Locate every cell, classifying each as a parasitized red blood cell, an uninfected red blood cell, or a white blood cell.
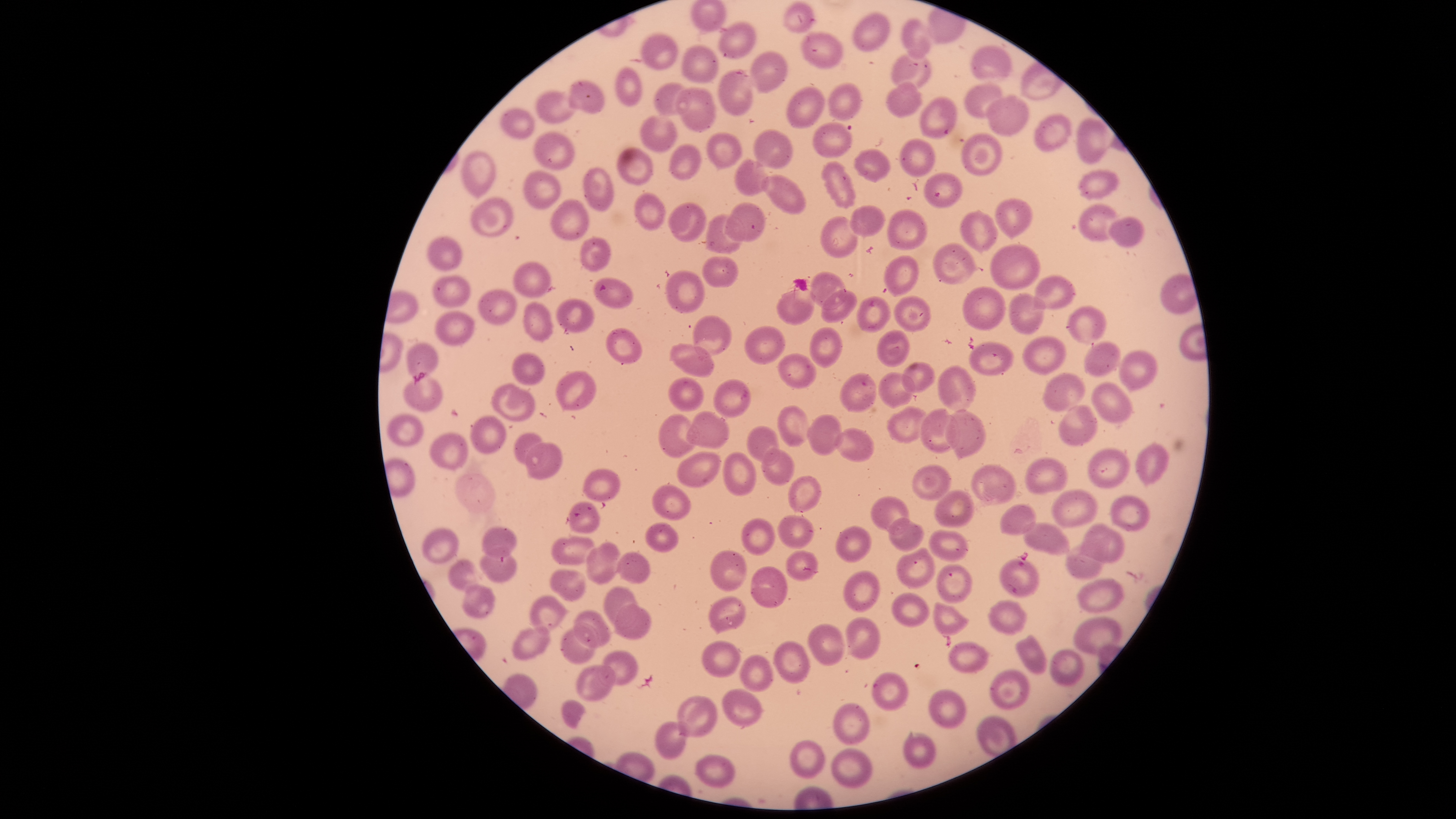
Approximate bounding boxes, in pixels from the top-left corner.
Parasitized red blood cells: (left=1000, top=557, right=1038, bottom=597).
Uninfected red blood cells: (left=690, top=0, right=727, bottom=32), (left=781, top=1, right=816, bottom=35), (left=852, top=13, right=891, bottom=53), (left=901, top=18, right=931, bottom=61), (left=718, top=22, right=757, bottom=59), (left=639, top=31, right=678, bottom=71), (left=800, top=31, right=844, bottom=69), (left=681, top=45, right=718, bottom=83), (left=971, top=45, right=1013, bottom=81), (left=750, top=51, right=787, bottom=93), (left=891, top=53, right=930, bottom=90), (left=615, top=68, right=643, bottom=106), (left=718, top=69, right=754, bottom=117), (left=567, top=80, right=606, bottom=114), (left=886, top=81, right=923, bottom=118), (left=653, top=82, right=693, bottom=117), (left=827, top=82, right=861, bottom=121), (left=962, top=84, right=1002, bottom=118), (left=786, top=86, right=825, bottom=130), (left=674, top=88, right=716, bottom=132), (left=536, top=90, right=577, bottom=124), (left=984, top=94, right=1029, bottom=136), (left=920, top=96, right=959, bottom=139), (left=499, top=108, right=536, bottom=140), (left=1034, top=113, right=1072, bottom=153), (left=639, top=114, right=678, bottom=153), (left=1076, top=118, right=1107, bottom=165), (left=813, top=122, right=852, bottom=158), (left=752, top=128, right=793, bottom=169), (left=534, top=131, right=575, bottom=170), (left=706, top=132, right=742, bottom=172), (left=961, top=133, right=1002, bottom=177), (left=899, top=139, right=935, bottom=178), (left=669, top=143, right=701, bottom=181), (left=617, top=147, right=653, bottom=186), (left=853, top=148, right=891, bottom=183), (left=461, top=150, right=498, bottom=199), (left=735, top=159, right=770, bottom=197), (left=820, top=160, right=856, bottom=210), (left=583, top=167, right=614, bottom=212), (left=1077, top=169, right=1119, bottom=200), (left=523, top=170, right=561, bottom=210), (left=923, top=171, right=964, bottom=209), (left=760, top=174, right=805, bottom=214), (left=633, top=192, right=667, bottom=231), (left=470, top=197, right=514, bottom=237), (left=995, top=198, right=1033, bottom=239), (left=551, top=199, right=590, bottom=241), (left=668, top=202, right=707, bottom=242), (left=724, top=202, right=766, bottom=242), (left=1079, top=204, right=1121, bottom=241), (left=850, top=205, right=885, bottom=240), (left=888, top=208, right=927, bottom=251), (left=960, top=209, right=999, bottom=256), (left=705, top=214, right=745, bottom=254), (left=821, top=216, right=858, bottom=258), (left=1108, top=217, right=1145, bottom=247), (left=426, top=234, right=461, bottom=271), (left=580, top=239, right=612, bottom=271), (left=931, top=243, right=979, bottom=285), (left=990, top=244, right=1040, bottom=290), (left=883, top=255, right=919, bottom=297), (left=701, top=256, right=739, bottom=288), (left=513, top=262, right=553, bottom=298), (left=664, top=269, right=705, bottom=314), (left=809, top=271, right=847, bottom=309), (left=432, top=275, right=471, bottom=307), (left=1033, top=275, right=1076, bottom=311), (left=593, top=277, right=634, bottom=310), (left=962, top=286, right=1006, bottom=331), (left=777, top=289, right=816, bottom=326), (left=477, top=290, right=517, bottom=325), (left=820, top=290, right=857, bottom=323), (left=1008, top=293, right=1046, bottom=334), (left=894, top=294, right=931, bottom=333), (left=856, top=296, right=891, bottom=333), (left=557, top=299, right=594, bottom=333), (left=522, top=301, right=554, bottom=342), (left=1067, top=304, right=1107, bottom=345), (left=433, top=311, right=476, bottom=346), (left=691, top=314, right=732, bottom=355), (left=744, top=325, right=785, bottom=365), (left=809, top=326, right=843, bottom=369), (left=606, top=328, right=644, bottom=365), (left=877, top=330, right=910, bottom=367), (left=1022, top=335, right=1067, bottom=376), (left=406, top=341, right=439, bottom=381), (left=969, top=341, right=1013, bottom=376), (left=1083, top=341, right=1121, bottom=376), (left=669, top=342, right=716, bottom=379), (left=1118, top=349, right=1158, bottom=394), (left=511, top=353, right=545, bottom=385), (left=777, top=353, right=816, bottom=389), (left=901, top=362, right=936, bottom=393), (left=937, top=365, right=977, bottom=413), (left=556, top=371, right=596, bottom=411), (left=839, top=372, right=877, bottom=413), (left=879, top=372, right=914, bottom=408), (left=404, top=373, right=444, bottom=413), (left=1042, top=373, right=1086, bottom=413), (left=668, top=376, right=705, bottom=413), (left=713, top=378, right=751, bottom=418), (left=1091, top=382, right=1133, bottom=423), (left=491, top=384, right=534, bottom=423), (left=1059, top=404, right=1098, bottom=448), (left=776, top=405, right=809, bottom=447), (left=887, top=406, right=927, bottom=444), (left=920, top=408, right=960, bottom=455), (left=946, top=408, right=986, bottom=462), (left=685, top=411, right=730, bottom=449), (left=658, top=413, right=698, bottom=459), (left=386, top=414, right=424, bottom=447), (left=807, top=414, right=842, bottom=455), (left=469, top=415, right=507, bottom=455), (left=746, top=425, right=780, bottom=466), (left=835, top=428, right=874, bottom=462), (left=430, top=431, right=469, bottom=471), (left=514, top=432, right=544, bottom=465), (left=525, top=441, right=563, bottom=479), (left=1135, top=442, right=1170, bottom=485), (left=761, top=448, right=795, bottom=486), (left=1088, top=449, right=1131, bottom=488), (left=676, top=452, right=721, bottom=487), (left=724, top=453, right=756, bottom=496), (left=1025, top=457, right=1068, bottom=494), (left=971, top=463, right=1016, bottom=506), (left=911, top=464, right=951, bottom=502), (left=582, top=468, right=621, bottom=503), (left=787, top=475, right=822, bottom=513), (left=651, top=484, right=691, bottom=520), (left=1051, top=490, right=1099, bottom=529), (left=935, top=491, right=975, bottom=525), (left=1109, top=494, right=1151, bottom=532), (left=870, top=496, right=911, bottom=535), (left=568, top=503, right=600, bottom=533), (left=1001, top=505, right=1036, bottom=534), (left=777, top=514, right=815, bottom=549), (left=740, top=515, right=775, bottom=556), (left=888, top=517, right=924, bottom=552), (left=645, top=522, right=680, bottom=552), (left=1022, top=522, right=1071, bottom=555), (left=1078, top=523, right=1125, bottom=563), (left=481, top=525, right=518, bottom=560), (left=836, top=526, right=872, bottom=563), (left=422, top=527, right=459, bottom=564), (left=928, top=531, right=967, bottom=560), (left=550, top=536, right=594, bottom=566), (left=585, top=541, right=621, bottom=586), (left=1065, top=542, right=1105, bottom=580), (left=897, top=547, right=935, bottom=589), (left=479, top=549, right=518, bottom=586), (left=710, top=549, right=748, bottom=592), (left=785, top=550, right=818, bottom=581), (left=617, top=552, right=649, bottom=584), (left=446, top=559, right=477, bottom=590), (left=936, top=563, right=973, bottom=604), (left=750, top=566, right=787, bottom=609), (left=550, top=570, right=587, bottom=601), (left=843, top=570, right=880, bottom=613), (left=1076, top=579, right=1123, bottom=614), (left=461, top=583, right=497, bottom=620), (left=604, top=586, right=640, bottom=628), (left=890, top=591, right=929, bottom=628), (left=529, top=596, right=570, bottom=634), (left=709, top=596, right=746, bottom=635), (left=987, top=600, right=1026, bottom=635), (left=613, top=601, right=652, bottom=640), (left=933, top=602, right=969, bottom=636), (left=572, top=609, right=612, bottom=649), (left=845, top=617, right=882, bottom=661), (left=1074, top=617, right=1122, bottom=655), (left=807, top=623, right=845, bottom=666), (left=560, top=625, right=598, bottom=665), (left=511, top=627, right=550, bottom=661), (left=1015, top=634, right=1048, bottom=674), (left=772, top=640, right=811, bottom=685), (left=701, top=641, right=740, bottom=678), (left=948, top=641, right=989, bottom=675), (left=1050, top=649, right=1084, bottom=687), (left=602, top=650, right=639, bottom=685), (left=739, top=653, right=773, bottom=692), (left=575, top=664, right=616, bottom=702), (left=990, top=670, right=1030, bottom=712), (left=872, top=671, right=908, bottom=712), (left=722, top=687, right=766, bottom=727), (left=929, top=688, right=967, bottom=729), (left=677, top=694, right=719, bottom=738), (left=561, top=699, right=586, bottom=729), (left=833, top=702, right=870, bottom=746), (left=654, top=721, right=689, bottom=759), (left=903, top=732, right=937, bottom=769), (left=790, top=740, right=827, bottom=779), (left=831, top=748, right=873, bottom=789), (left=695, top=755, right=737, bottom=789).
No white blood cells identified.

Species: Plasmodium falciparum. The visible region is circular. Single field of view. Image is 1456×819 pixels. Giemsa-stained preparation. Smartphone photograph through the microscope eyepiece. Thin blood smear.